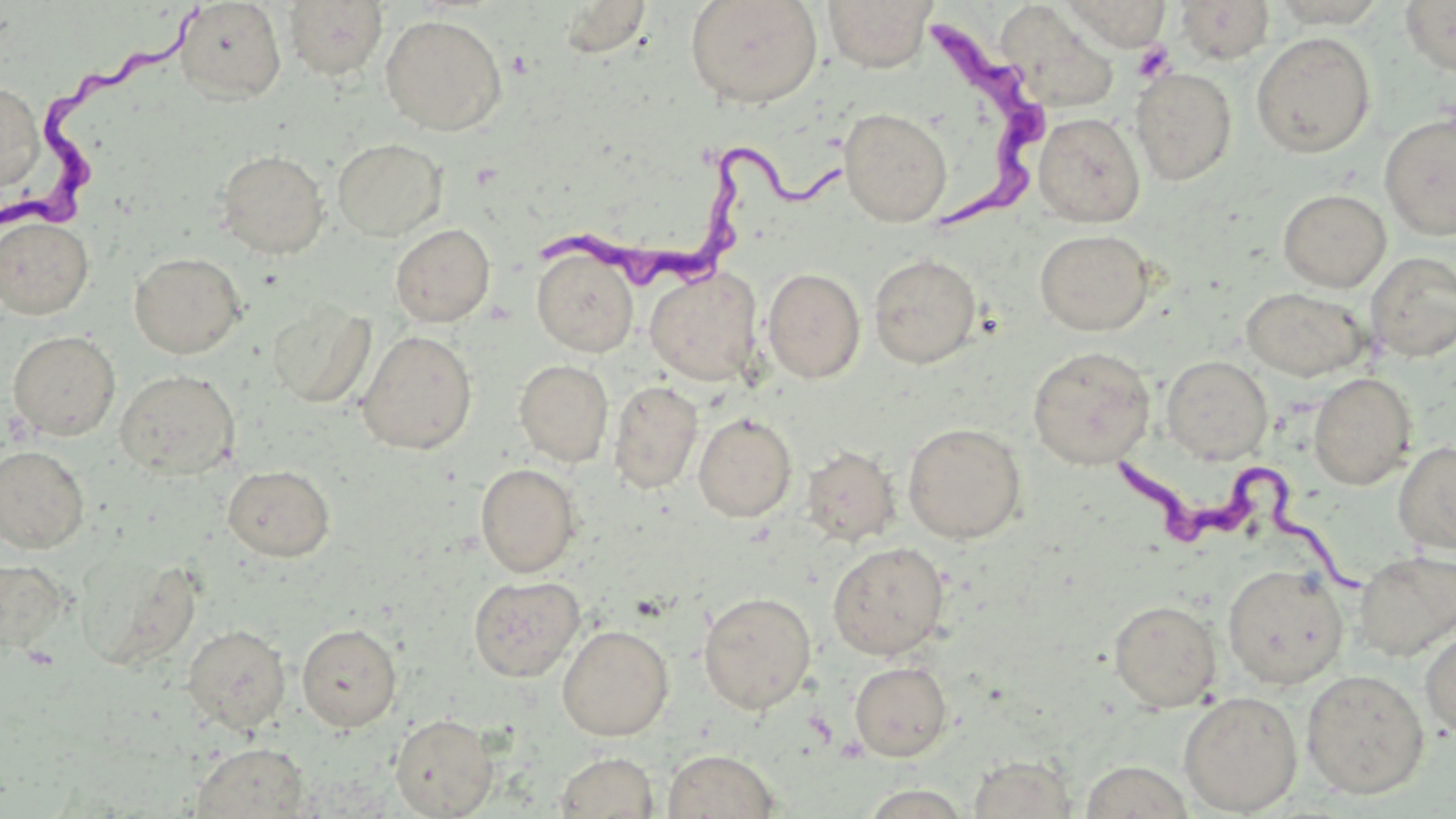
slide-level diagnosis = Trypanosoma brucei
magnification = 1000x
uninfected red blood cell locations = approximate bounding boxes as [x1, y1, x2, y2] in pixels: [685, 0, 823, 108], [822, 0, 937, 73], [1061, 0, 1170, 51], [1175, 0, 1275, 65], [1399, 0, 1456, 77], [174, 1, 287, 104], [284, 1, 388, 81], [558, 1, 654, 58], [1266, 1, 1390, 28], [997, 6, 1121, 115], [380, 14, 507, 136], [1251, 32, 1375, 158], [1131, 66, 1237, 185], [0, 81, 44, 192], [839, 108, 952, 226], [1033, 112, 1145, 227], [1378, 112, 1456, 240], [332, 138, 447, 241], [216, 149, 330, 259], [1277, 188, 1391, 292], [0, 215, 94, 318], [390, 223, 495, 327], [1035, 229, 1154, 336], [531, 248, 639, 357], [1365, 251, 1456, 362], [129, 252, 245, 358], [869, 253, 981, 368], [644, 266, 763, 386], [762, 267, 866, 384], [1242, 287, 1370, 381], [267, 303, 375, 408], [7, 330, 120, 440], [357, 330, 478, 454], [4, 331, 100, 553], [1027, 346, 1156, 469], [1161, 355, 1272, 463], [514, 359, 613, 467], [115, 369, 240, 480], [1308, 372, 1417, 489], [608, 381, 703, 494], [693, 413, 797, 522], [903, 423, 1027, 543], [1394, 441, 1456, 555], [0, 445, 90, 554], [801, 445, 900, 546], [475, 463, 582, 577], [223, 465, 334, 562], [827, 541, 949, 660], [1354, 549, 1456, 660], [79, 552, 204, 670], [0, 557, 69, 654], [1223, 564, 1348, 689], [468, 575, 585, 682], [698, 591, 816, 714], [1109, 599, 1222, 712], [296, 623, 402, 731], [182, 624, 291, 734], [557, 624, 674, 740], [1420, 625, 1456, 742], [850, 661, 953, 761], [1301, 668, 1429, 799], [1178, 690, 1303, 816], [390, 713, 498, 818], [191, 742, 311, 818], [662, 748, 780, 819], [553, 751, 659, 819], [967, 755, 1077, 818], [1079, 761, 1195, 818], [858, 784, 973, 818]
field of view = single
preparation = thin blood film
Trypanosoma brucei locations = approximate bounding boxes as [x1, y1, x2, y2] in pixels: [3, 3, 208, 237], [914, 10, 1042, 229], [535, 144, 843, 290], [1107, 442, 1369, 601]
platelet locations = approximate bounding boxes as [x1, y1, x2, y2] in pixels: [1133, 42, 1176, 83]
stain = May-Grünwald-Giemsa
modality = light microscopy
image size = 1456×819 pixels